State which cell type is depicted.
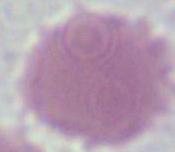
An erythrocyte.

1000x magnification. Photomicrograph.